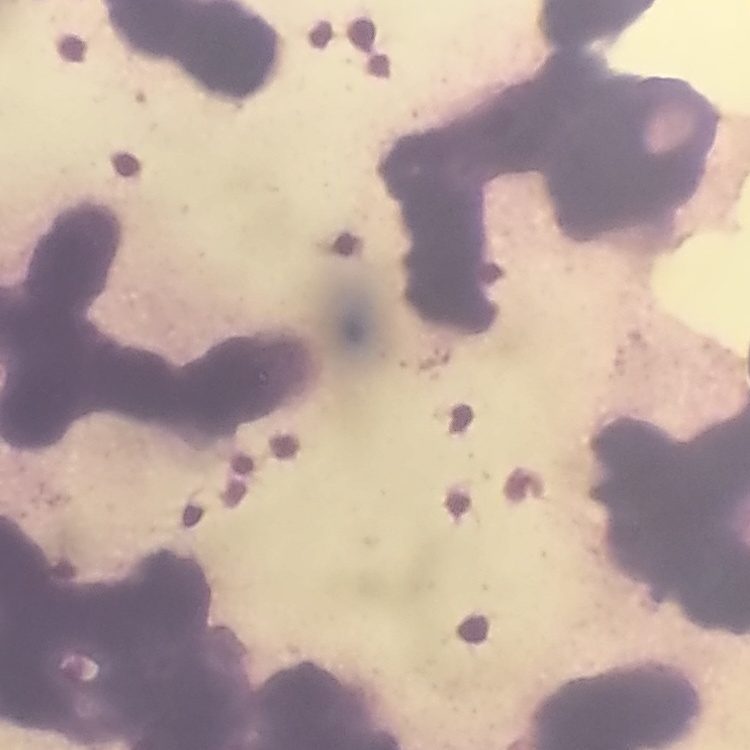

Summary:
  - Erythrocyte morphology: rouleaux formation
  - Stain: Field's or Giemsa
  - Preparation: thin blood film
  - Image type: one tile cut from a larger photomicrograph